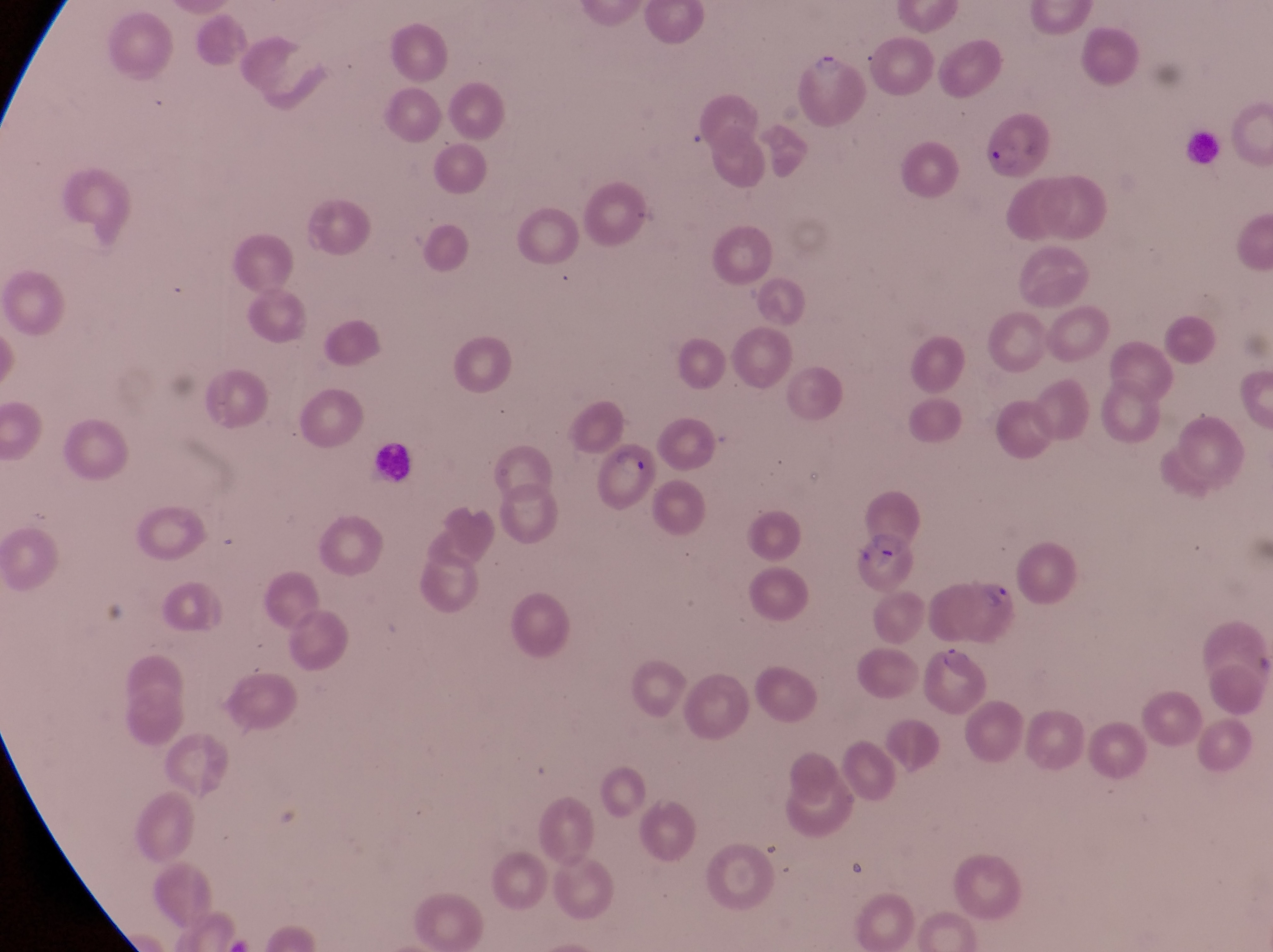

Approximate bounding boxes as left top right bottom in pixels. Parasitised red blood cell locations: 791 43 868 128; 981 98 1053 176; 596 442 663 517; 856 479 926 559; 936 570 1018 645; 923 647 990 712. Leukocyte locations: 1183 134 1233 174; 372 437 419 494. At a magnification of 1000x. Captured by a smartphone held over the eyepiece of an Olympus CX-23 microscope. Image is 1273×952 pixels. One field of view. Collected in Uganda. Thin blood film.